Locate every blood parasite and identify its species.
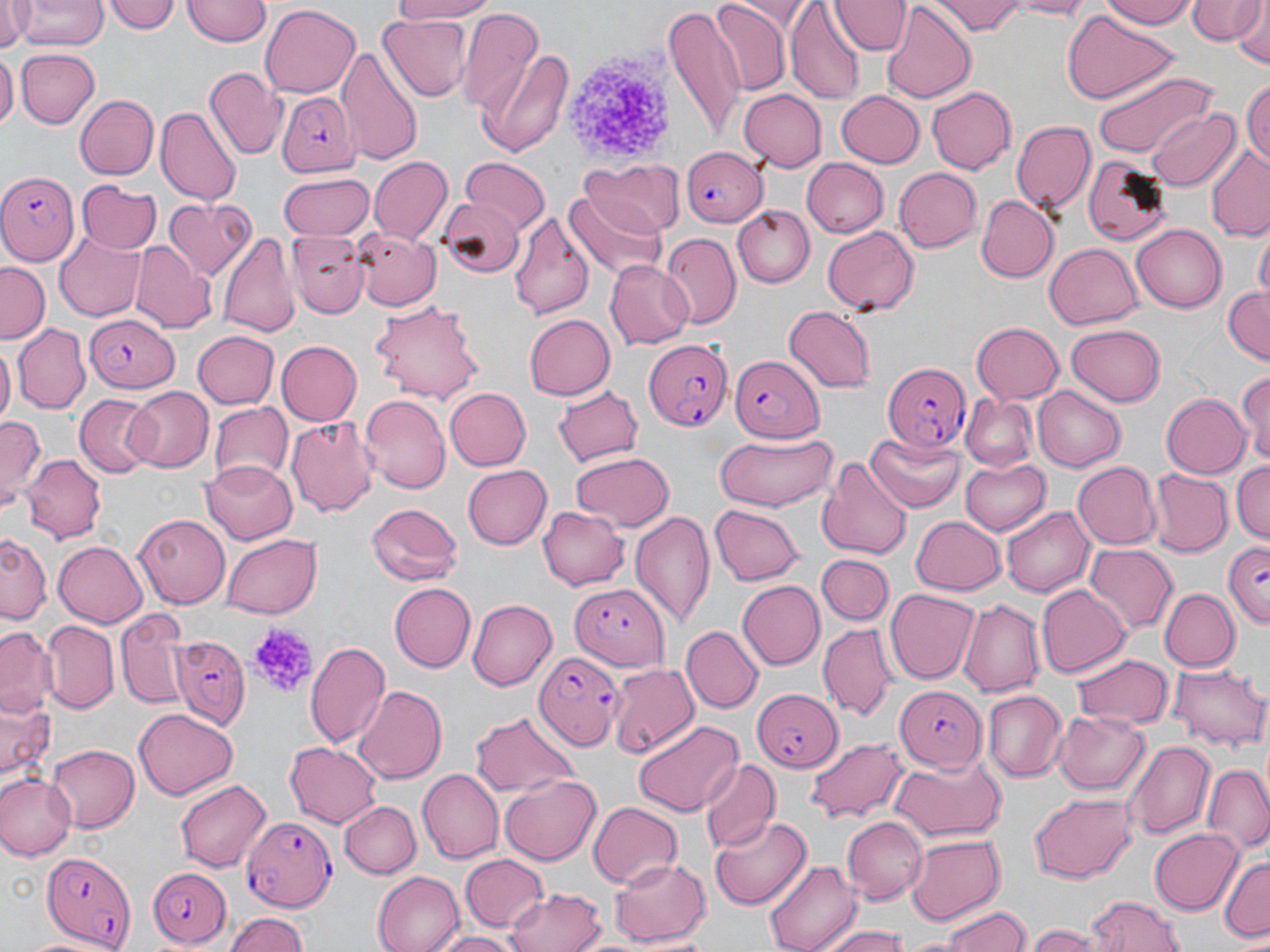

Approximate bounding boxes as named x1/y1/x2/y2 corners in pixels.
Plasmodium falciparum-infected red blood cells: (x1=278, y1=90, x2=360, y2=179), (x1=680, y1=146, x2=768, y2=226), (x1=0, y1=170, x2=80, y2=265), (x1=86, y1=317, x2=181, y2=395), (x1=643, y1=337, x2=734, y2=432), (x1=730, y1=352, x2=826, y2=442), (x1=881, y1=363, x2=972, y2=453), (x1=1223, y1=540, x2=1270, y2=627), (x1=569, y1=582, x2=670, y2=670), (x1=172, y1=635, x2=253, y2=727), (x1=533, y1=648, x2=624, y2=751), (x1=748, y1=685, x2=843, y2=778), (x1=894, y1=686, x2=986, y2=770), (x1=243, y1=818, x2=336, y2=908), (x1=42, y1=850, x2=132, y2=948), (x1=150, y1=864, x2=233, y2=951).
No Plasmodium ovale, Plasmodium malariae, Plasmodium vivax, Babesia divergens, or Trypanosoma brucei observed.

{
  "slide_level_diagnosis": "Plasmodium falciparum",
  "stain": "May-Grünwald-Giemsa",
  "modality": "optical microscopy",
  "platelet_locations": "approximate bounding boxes as named x1/y1/x2/y2 corners in pixels: (x1=561, y1=47, x2=672, y2=168), (x1=243, y1=620, x2=318, y2=701)",
  "magnification": "1000x",
  "uninfected_red_blood_cell_locations": "approximate bounding boxes as named x1/y1/x2/y2 corners in pixels: (x1=2, y1=0, x2=33, y2=51), (x1=107, y1=0, x2=180, y2=34), (x1=384, y1=0, x2=500, y2=24), (x1=833, y1=0, x2=907, y2=54), (x1=933, y1=0, x2=1025, y2=36), (x1=1001, y1=0, x2=1100, y2=18), (x1=1103, y1=0, x2=1201, y2=28), (x1=1187, y1=0, x2=1266, y2=46), (x1=16, y1=1, x2=106, y2=51), (x1=182, y1=1, x2=270, y2=48), (x1=712, y1=2, x2=793, y2=93), (x1=881, y1=2, x2=976, y2=104), (x1=1230, y1=2, x2=1268, y2=70), (x1=785, y1=3, x2=864, y2=104), (x1=258, y1=4, x2=360, y2=98), (x1=662, y1=4, x2=745, y2=144), (x1=457, y1=10, x2=544, y2=114), (x1=1061, y1=10, x2=1176, y2=104), (x1=377, y1=15, x2=469, y2=102), (x1=476, y1=45, x2=575, y2=160), (x1=337, y1=46, x2=423, y2=163), (x1=17, y1=47, x2=98, y2=130), (x1=0, y1=50, x2=15, y2=135), (x1=1091, y1=67, x2=1217, y2=159), (x1=204, y1=69, x2=286, y2=159), (x1=1243, y1=75, x2=1270, y2=173), (x1=927, y1=87, x2=1017, y2=174), (x1=739, y1=88, x2=827, y2=172), (x1=835, y1=90, x2=924, y2=169), (x1=74, y1=93, x2=159, y2=181), (x1=156, y1=106, x2=241, y2=207), (x1=1146, y1=106, x2=1239, y2=192), (x1=1010, y1=119, x2=1096, y2=217), (x1=1204, y1=150, x2=1270, y2=242), (x1=1082, y1=155, x2=1175, y2=244), (x1=368, y1=157, x2=454, y2=245), (x1=458, y1=158, x2=550, y2=231), (x1=805, y1=158, x2=888, y2=237), (x1=581, y1=159, x2=679, y2=236), (x1=893, y1=168, x2=984, y2=253), (x1=278, y1=174, x2=374, y2=242), (x1=77, y1=181, x2=161, y2=252), (x1=568, y1=187, x2=667, y2=279), (x1=439, y1=194, x2=523, y2=275), (x1=977, y1=194, x2=1057, y2=281), (x1=164, y1=197, x2=257, y2=281), (x1=734, y1=205, x2=816, y2=288), (x1=510, y1=211, x2=594, y2=321), (x1=1131, y1=224, x2=1227, y2=312), (x1=821, y1=226, x2=920, y2=315), (x1=354, y1=228, x2=444, y2=314), (x1=55, y1=229, x2=144, y2=322), (x1=218, y1=229, x2=301, y2=341), (x1=288, y1=231, x2=370, y2=318), (x1=661, y1=232, x2=742, y2=329), (x1=1254, y1=232, x2=1269, y2=305), (x1=129, y1=243, x2=215, y2=331), (x1=1044, y1=243, x2=1144, y2=330), (x1=0, y1=260, x2=50, y2=340), (x1=604, y1=261, x2=695, y2=349), (x1=1222, y1=285, x2=1270, y2=364), (x1=371, y1=300, x2=484, y2=401), (x1=783, y1=305, x2=879, y2=392), (x1=524, y1=314, x2=617, y2=400), (x1=971, y1=322, x2=1064, y2=403), (x1=14, y1=324, x2=89, y2=413), (x1=1065, y1=324, x2=1167, y2=407), (x1=191, y1=331, x2=277, y2=410), (x1=277, y1=340, x2=362, y2=425), (x1=0, y1=341, x2=15, y2=428), (x1=1237, y1=368, x2=1270, y2=471), (x1=551, y1=384, x2=645, y2=463), (x1=125, y1=387, x2=211, y2=472), (x1=1034, y1=387, x2=1124, y2=471), (x1=443, y1=388, x2=529, y2=471), (x1=1161, y1=391, x2=1253, y2=479), (x1=360, y1=394, x2=450, y2=493), (x1=74, y1=395, x2=157, y2=477), (x1=961, y1=395, x2=1039, y2=472), (x1=208, y1=403, x2=291, y2=486), (x1=0, y1=413, x2=45, y2=506), (x1=287, y1=414, x2=380, y2=518), (x1=710, y1=430, x2=838, y2=512), (x1=866, y1=431, x2=964, y2=512), (x1=569, y1=451, x2=676, y2=530), (x1=21, y1=452, x2=104, y2=540), (x1=960, y1=456, x2=1052, y2=536), (x1=816, y1=457, x2=913, y2=561), (x1=1233, y1=459, x2=1269, y2=548), (x1=200, y1=461, x2=297, y2=542), (x1=1072, y1=461, x2=1161, y2=549), (x1=461, y1=465, x2=551, y2=550), (x1=1149, y1=470, x2=1233, y2=556), (x1=365, y1=501, x2=465, y2=586), (x1=538, y1=505, x2=628, y2=590), (x1=709, y1=505, x2=802, y2=584), (x1=1003, y1=505, x2=1094, y2=598), (x1=630, y1=511, x2=716, y2=632), (x1=910, y1=513, x2=1007, y2=594), (x1=133, y1=514, x2=230, y2=609), (x1=0, y1=533, x2=49, y2=625), (x1=222, y1=534, x2=323, y2=618), (x1=52, y1=540, x2=148, y2=629), (x1=1084, y1=543, x2=1178, y2=637), (x1=818, y1=554, x2=894, y2=627), (x1=739, y1=580, x2=824, y2=671), (x1=391, y1=582, x2=476, y2=672), (x1=1037, y1=584, x2=1130, y2=678), (x1=1159, y1=588, x2=1239, y2=673), (x1=885, y1=589, x2=979, y2=684), (x1=467, y1=597, x2=558, y2=690), (x1=958, y1=599, x2=1044, y2=697), (x1=116, y1=610, x2=187, y2=711), (x1=43, y1=621, x2=117, y2=712), (x1=817, y1=622, x2=897, y2=721), (x1=1, y1=623, x2=59, y2=721), (x1=682, y1=626, x2=762, y2=712), (x1=306, y1=643, x2=390, y2=751), (x1=1072, y1=652, x2=1170, y2=727), (x1=609, y1=663, x2=699, y2=758), (x1=1170, y1=663, x2=1267, y2=750), (x1=354, y1=687, x2=447, y2=782), (x1=982, y1=690, x2=1066, y2=782), (x1=1, y1=694, x2=57, y2=793), (x1=135, y1=708, x2=238, y2=799), (x1=1052, y1=708, x2=1151, y2=796), (x1=468, y1=709, x2=581, y2=797), (x1=631, y1=720, x2=743, y2=818), (x1=806, y1=737, x2=910, y2=822), (x1=287, y1=739, x2=384, y2=828), (x1=1126, y1=739, x2=1216, y2=841), (x1=47, y1=744, x2=139, y2=832), (x1=312, y1=754, x2=411, y2=856), (x1=888, y1=754, x2=1009, y2=843), (x1=698, y1=757, x2=779, y2=855), (x1=1202, y1=764, x2=1270, y2=855), (x1=418, y1=768, x2=506, y2=863), (x1=0, y1=773, x2=76, y2=861), (x1=500, y1=773, x2=601, y2=866), (x1=173, y1=777, x2=272, y2=872), (x1=1027, y1=793, x2=1137, y2=882), (x1=340, y1=799, x2=421, y2=878), (x1=587, y1=802, x2=682, y2=888), (x1=709, y1=815, x2=813, y2=911), (x1=841, y1=816, x2=926, y2=901), (x1=1149, y1=827, x2=1244, y2=915), (x1=903, y1=832, x2=1005, y2=925), (x1=460, y1=854, x2=546, y2=931), (x1=1218, y1=854, x2=1270, y2=944), (x1=608, y1=856, x2=711, y2=945), (x1=763, y1=858, x2=862, y2=952), (x1=372, y1=870, x2=463, y2=951), (x1=504, y1=885, x2=609, y2=952), (x1=1086, y1=895, x2=1184, y2=952), (x1=939, y1=904, x2=1031, y2=951), (x1=222, y1=911, x2=310, y2=952), (x1=818, y1=925, x2=913, y2=952), (x1=1027, y1=926, x2=1095, y2=950), (x1=431, y1=930, x2=518, y2=952)",
  "field_of_view": "one of a larger specimen",
  "image_size": "1270×952 pixels",
  "preparation": "thin blood smear"
}